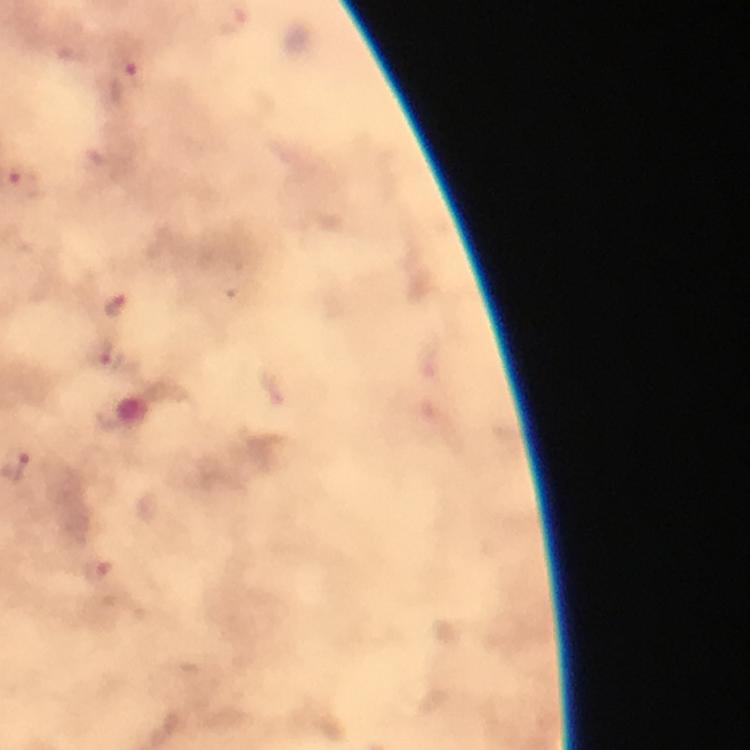
Approximate centers as {x, y} in pixels. Malaria parasite locations: {126, 77}, {23, 182}, {115, 306}. Immersion oil applied. From a diagnostic examination for malaria. A crop from one field of view. Photographed through the microscope with a smartphone camera. Image is 750×750 pixels. 100x magnification. Thick blood film. Giemsa stain.